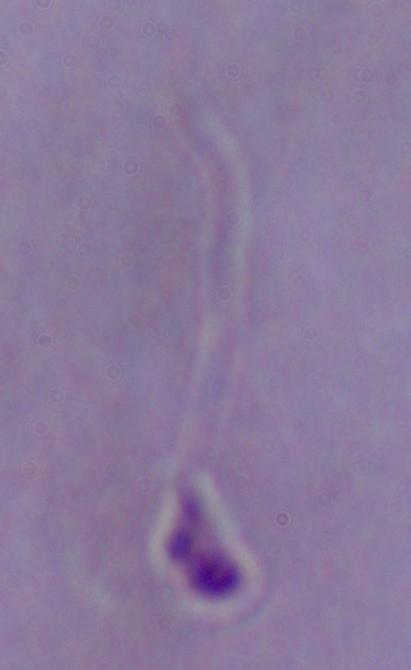

Captured at 1000x magnification. Micrograph. A Leishmania parasite is seen.